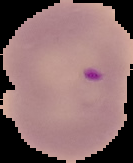
Image is 133×163 pixels. Cell region segmented out of the field of view; the surrounding area is masked to black. From a thin blood smear. Result: Plasmodium parasites identified.